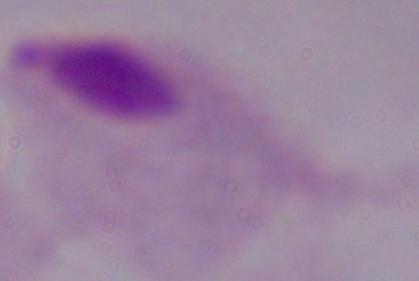
Summary:
  - Modality: photomicrograph
  - Identification: trichomonad
  - Magnification: 1000x